Report the malaria status of this cell.
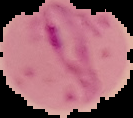

It is parasitized.

preparation = thin blood smear
image type = segmented cell region with the area outside set to black
image size = 133×118 pixels